Locate every leukocyte (white blood cell).
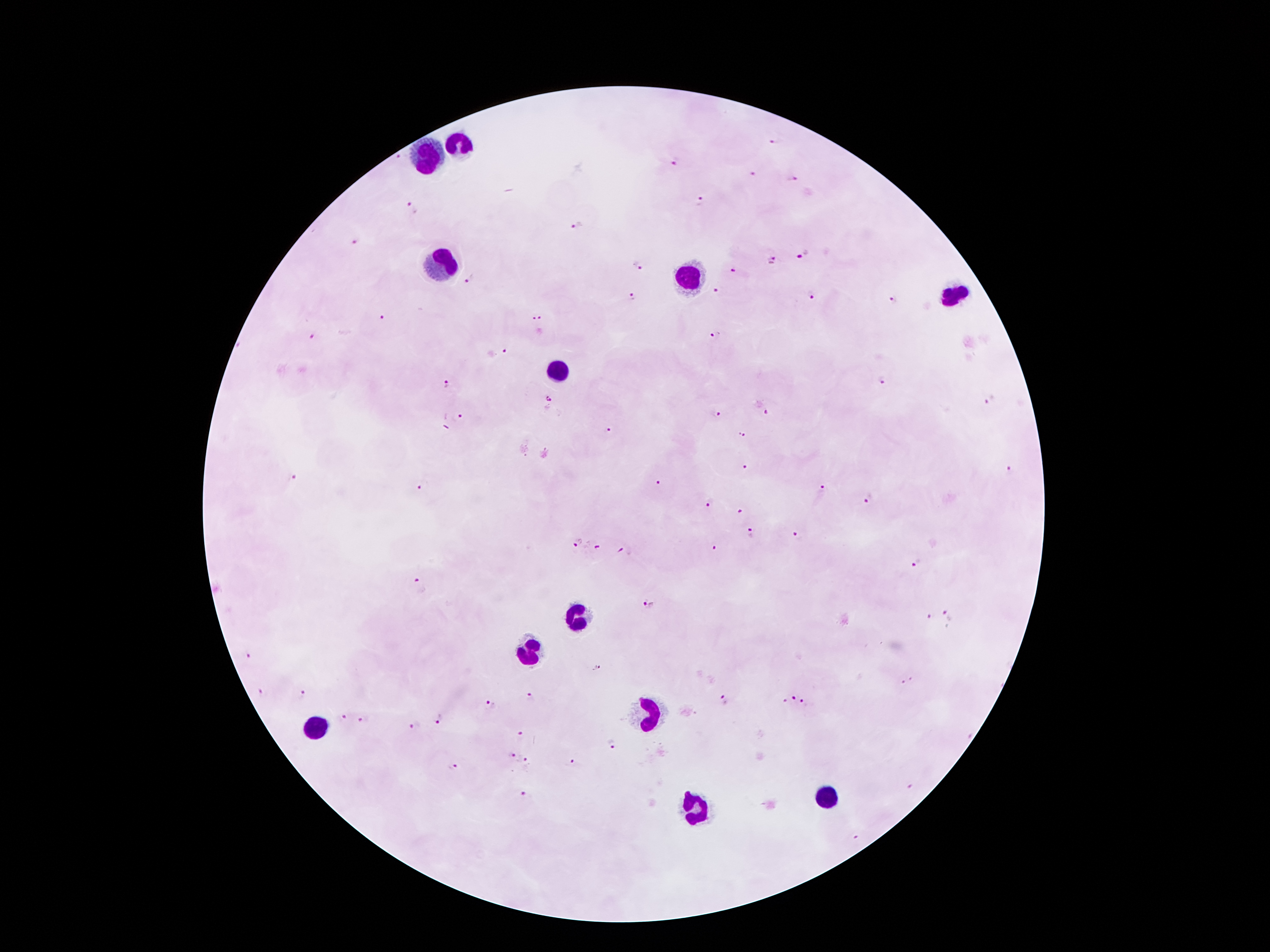

Approximate centers as [x, y] in pixels.
Leukocytes: [465, 142], [425, 159], [445, 261], [695, 276], [957, 297], [556, 375], [573, 618], [529, 649], [650, 714], [316, 726], [830, 798], [692, 809].

Plasmodium parasite locations = [775, 141], [397, 157], [675, 164], [752, 175], [790, 179], [701, 201], [411, 208], [577, 227], [355, 241], [803, 254], [771, 261], [635, 266], [733, 268], [470, 280], [717, 292], [634, 297], [811, 298], [895, 300], [382, 318], [542, 318], [714, 336], [312, 338], [505, 349], [881, 380], [448, 382], [991, 399], [549, 403], [717, 413], [767, 413], [461, 415], [608, 430], [741, 435], [743, 466], [1010, 469], [294, 477], [659, 483], [822, 487], [419, 488], [868, 500], [709, 501], [739, 511], [751, 533], [794, 534], [577, 541], [598, 547], [713, 547], [626, 551], [915, 564], [419, 585], [648, 607], [948, 617], [932, 618], [248, 656], [597, 669], [909, 683], [260, 693], [302, 696], [793, 696], [531, 697], [786, 700], [722, 701], [490, 705], [806, 706], [341, 717], [439, 717], [365, 722], [414, 726], [521, 735], [611, 746], [509, 758], [574, 762], [526, 763], [452, 768], [911, 787], [526, 797], [857, 837]
preparation = thick peripheral-blood smear
patient malaria status = positive for Plasmodium falciparum
stain = Giemsa
magnification = 100x
capture = smartphone through the microscope eyepiece
field of view = one from this slide
image size = 1270×952 pixels